Assess this cell for malaria.
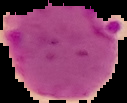
Parasitized.

image_size: 127×103 pixels
image_type: cell region segmented out of the field of view; surrounding area masked to black
preparation: thin blood smear